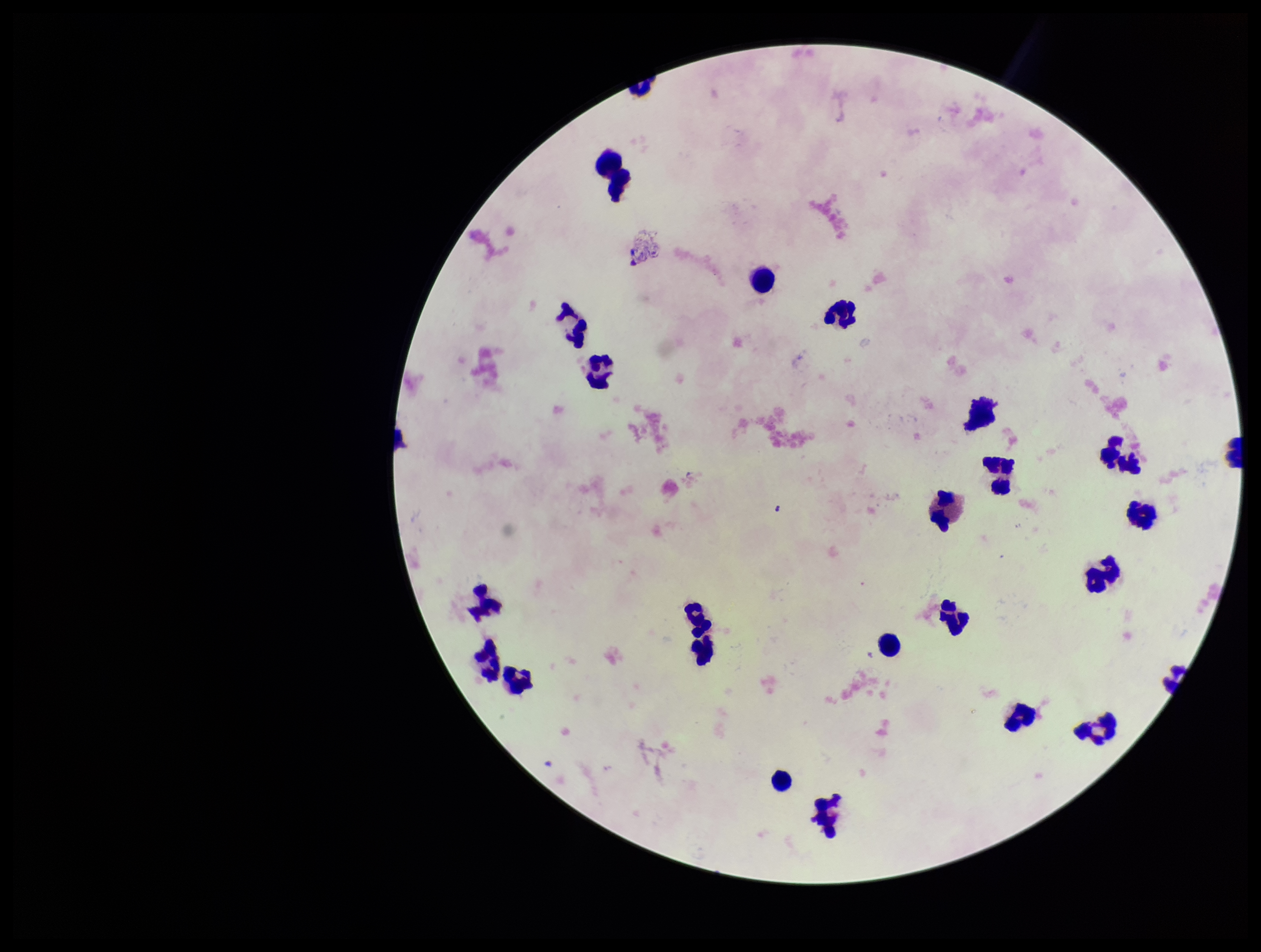
Summary:
  - Leukocyte count: 25
  - Patient malaria status: negative
  - Field of view: one from this slide
  - Preparation: thick smear
  - Plasmodium parasites: none seen
  - Image size: 1261×952 pixels
  - Capture: smartphone photograph through the microscope eyepiece
  - Stain: Giemsa
  - Parasite count: 0